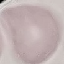
Result: no malaria parasites detected. Automatically extracted cell patch, resized to 64 × 64 pixels. Photographed with a smartphone camera at the microscope eyepiece. Giemsa stain. Thin blood film.